Locate every malaria parasite.
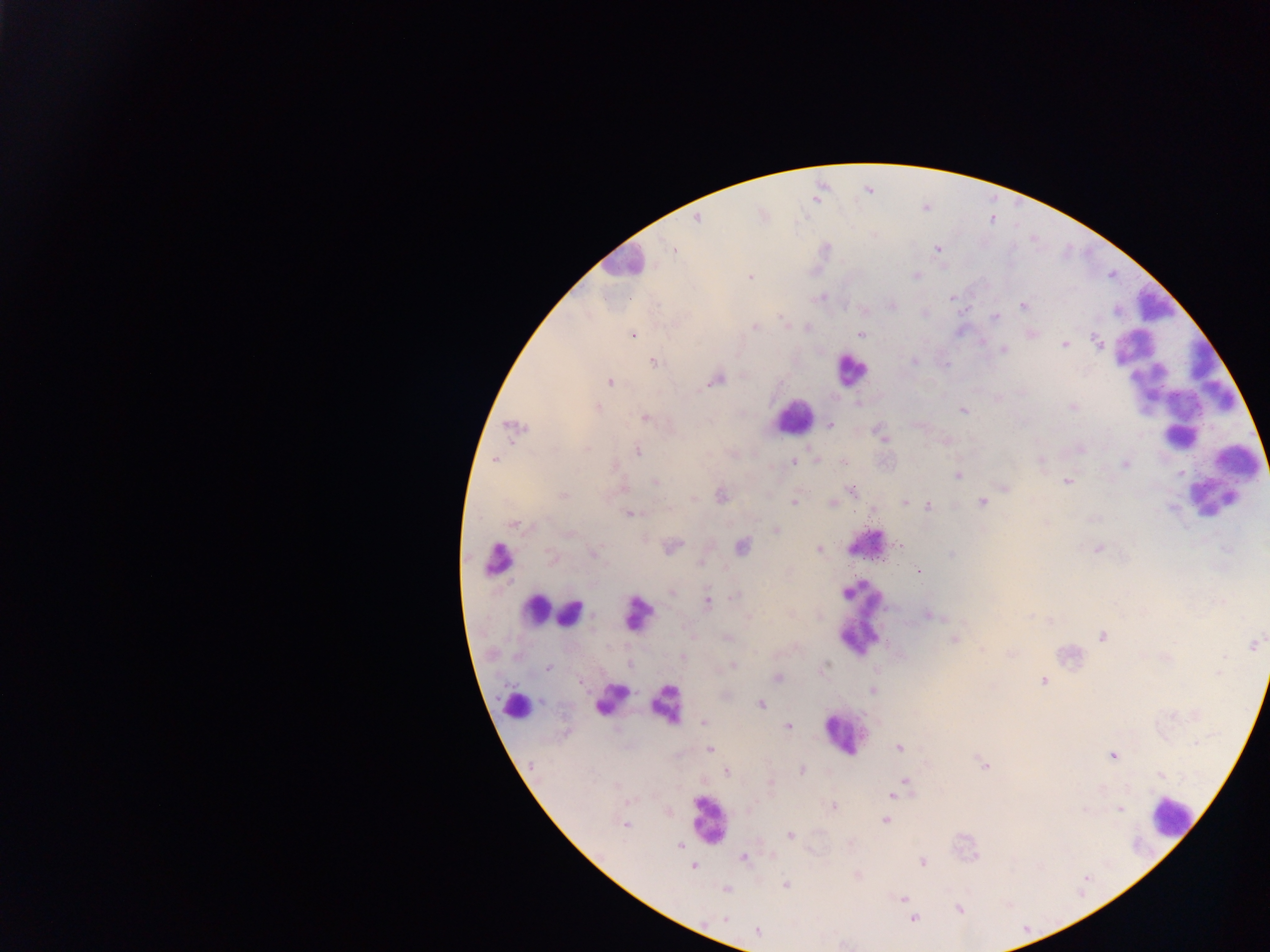
Approximate centers as {x, y} in pixels.
Malaria parasites: {696, 220}, {937, 248}, {673, 249}, {916, 276}, {750, 277}, {951, 298}, {1023, 305}, {892, 306}, {995, 317}, {781, 318}, {755, 327}, {633, 334}, {860, 334}, {1096, 342}, {1065, 345}, {1003, 350}, {915, 361}, {654, 362}, {716, 379}, {609, 382}, {598, 407}, {1073, 407}, {964, 410}, {646, 419}, {830, 425}, {516, 428}, {881, 434}, {1080, 449}, {588, 450}, {638, 452}, {495, 460}, {1040, 460}, {843, 461}, {794, 462}, {1125, 463}, {614, 466}, {957, 475}, {655, 481}, {1067, 482}, {1004, 488}, {852, 491}, {563, 495}, {720, 496}, {693, 499}, {795, 502}, {831, 502}, {905, 503}, {982, 503}, {928, 506}, {631, 514}, {514, 525}, {776, 530}, {569, 533}, {898, 545}, {742, 546}, {672, 547}, {1098, 548}, {819, 549}, {595, 553}, {951, 554}, {550, 556}, {701, 563}, {919, 571}, {672, 592}, {735, 595}, {708, 601}, {929, 616}, {748, 617}, {727, 637}, {1102, 637}, {954, 640}, {1253, 645}, {982, 650}, {683, 657}, {732, 665}, {547, 667}, {1219, 672}, {778, 678}, {1043, 681}, {581, 682}, {873, 690}, {761, 704}, {703, 722}, {788, 726}, {899, 747}, {710, 749}, {1112, 755}, {985, 765}, {802, 770}, {726, 772}, {904, 781}, {616, 785}, {897, 791}, {892, 794}, {834, 807}, {1120, 809}, {885, 820}, {625, 825}, {790, 834}, {679, 846}, {744, 857}, {923, 862}, {692, 866}, {785, 885}, {726, 889}, {903, 898}, {959, 909}, {725, 919}, {913, 919}, {757, 931}.

Summary:
  - Leukocyte locations: {620, 260}, {1155, 301}, {850, 370}, {1179, 397}, {793, 416}, {1223, 480}, {863, 535}, {492, 559}, {537, 610}, {569, 613}, {633, 615}, {861, 620}, {611, 699}, {516, 704}, {665, 706}, {842, 733}, {1172, 816}, {709, 819}
  - Field of view: single
  - Country: Ghana
  - Image size: 1270×952 pixels
  - Capture: mobile-phone photograph through a microscope
  - Preparation: thick blood film